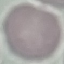

Summary:
  - Malaria status: uninfected
  - Stain: Giemsa
  - Capture: smartphone camera at the microscope eyepiece
  - Preparation: thin blood film
  - Image type: automatically extracted cell patch, resized to 64 × 64 pixels